Locate and identify every blood parasite.
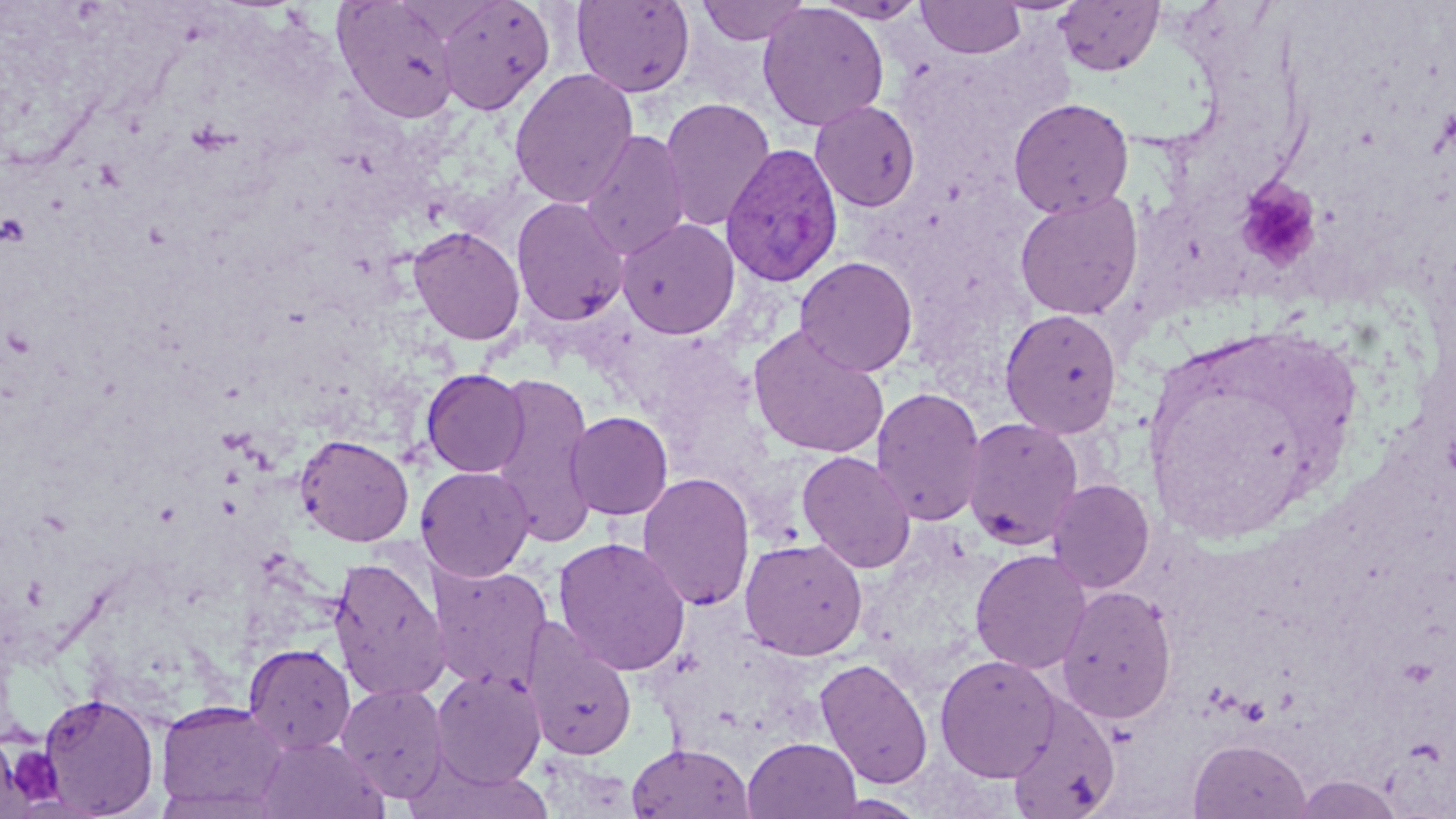

Approximate bounding boxes as [x1, y1, x2, y2] in pixels.
Plasmodium vivax-infected red blood cells: [721, 142, 843, 287].
No Plasmodium falciparum, Plasmodium ovale, Plasmodium malariae, Babesia divergens, or Trypanosoma brucei observed.

slide-level diagnosis = Plasmodium vivax
preparation = thin blood film
magnification = 1000x
modality = optical microscopy
field of view = one of a larger specimen
uninfected red blood cell locations = approximate bounding boxes as [x1, y1, x2, y2] in pixels: [332, 0, 462, 124], [435, 0, 555, 115], [571, 0, 695, 97], [695, 0, 811, 46], [813, 0, 929, 24], [917, 0, 1025, 59], [1054, 1, 1164, 77], [757, 2, 889, 131], [509, 68, 639, 209], [658, 97, 776, 232], [1008, 97, 1135, 219], [810, 100, 921, 212], [580, 129, 691, 261], [1014, 190, 1144, 320], [511, 196, 630, 328], [616, 217, 740, 339], [407, 225, 526, 345], [794, 256, 918, 377], [1000, 308, 1123, 438], [747, 325, 890, 459], [421, 368, 530, 477], [488, 371, 600, 549], [871, 386, 987, 526], [564, 411, 673, 519], [962, 416, 1085, 550], [294, 433, 414, 546], [796, 450, 917, 573], [415, 465, 535, 581], [636, 471, 756, 612], [1046, 478, 1155, 594], [552, 536, 691, 676], [739, 537, 868, 660], [969, 548, 1092, 674], [328, 556, 450, 701], [427, 562, 552, 693], [1056, 585, 1177, 724], [523, 623, 637, 762], [243, 643, 356, 755], [934, 654, 1061, 782], [814, 657, 933, 789], [431, 668, 546, 787], [336, 681, 450, 802], [38, 691, 160, 818], [1004, 696, 1121, 819], [155, 699, 289, 816], [256, 735, 387, 818], [743, 736, 863, 819], [1188, 738, 1312, 819], [625, 742, 754, 819], [1291, 775, 1403, 818], [819, 794, 929, 818]
stain = May-Grünwald-Giemsa
image size = 1456×819 pixels
platelet locations = approximate bounding boxes as [x1, y1, x2, y2] in pixels: [1235, 178, 1322, 272], [5, 745, 64, 806]